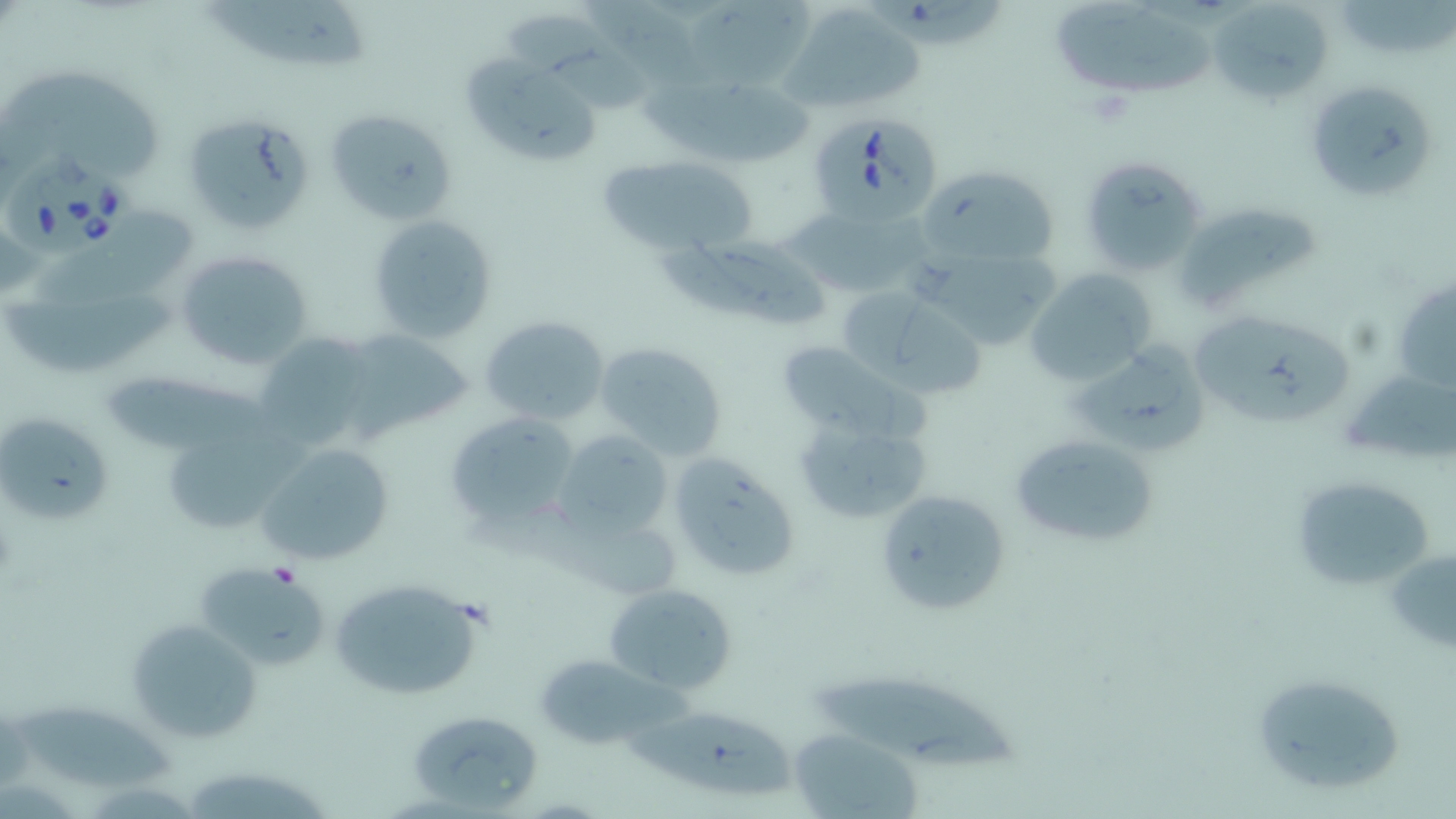
Summary:
  - Coordinate format: approximate bounding boxes as (x1, y1, x2, y2) in pixels
  - Uninfected red blood cell locations: (685, 0, 822, 90), (1053, 1, 1224, 95), (198, 2, 380, 72), (1206, 2, 1330, 105), (780, 4, 924, 112), (502, 10, 650, 106), (457, 50, 603, 167), (1, 71, 165, 182), (1304, 79, 1435, 203), (636, 80, 814, 163), (324, 107, 459, 229), (182, 110, 316, 236), (1079, 154, 1209, 277), (595, 155, 760, 255), (918, 165, 1063, 271), (1175, 199, 1325, 304), (367, 214, 497, 342), (781, 214, 937, 296), (31, 215, 195, 300), (667, 236, 837, 329), (175, 249, 313, 370), (909, 252, 1064, 352), (1024, 267, 1157, 387), (4, 293, 178, 380), (869, 296, 993, 405), (1187, 308, 1348, 425), (478, 314, 611, 425), (338, 326, 476, 441), (252, 333, 379, 453), (1069, 339, 1215, 454), (775, 340, 908, 436), (596, 341, 729, 461), (96, 373, 287, 458), (790, 407, 934, 527), (443, 410, 580, 533), (0, 411, 110, 530), (163, 427, 319, 530), (554, 430, 674, 543), (1009, 431, 1157, 549), (252, 442, 395, 567), (666, 453, 802, 583), (1289, 474, 1438, 591), (874, 488, 1010, 616), (1384, 543, 1456, 656), (198, 560, 329, 671), (330, 574, 488, 701), (603, 581, 739, 697), (126, 617, 262, 743), (534, 655, 669, 749), (808, 671, 1020, 774), (1248, 671, 1409, 799), (7, 700, 178, 792), (624, 707, 797, 798), (406, 709, 542, 813), (790, 729, 924, 818)
  - Babesia divergens-infected red blood cell locations: (805, 113, 944, 225), (1, 153, 132, 262)
  - Slide-level diagnosis: Babesia divergens
  - Magnification: 1000x
  - Preparation: thin blood film
  - Stain: May-Grünwald-Giemsa
  - Modality: optical microscopy
  - Field of view: one of a larger specimen
  - Image size: 1456×819 pixels